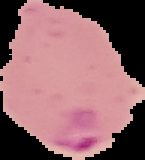

Summary:
  - Preparation: thin blood smear
  - Image type: segmented cell region on a black background
  - Image size: 145×160 pixels
  - Malaria status: parasitized